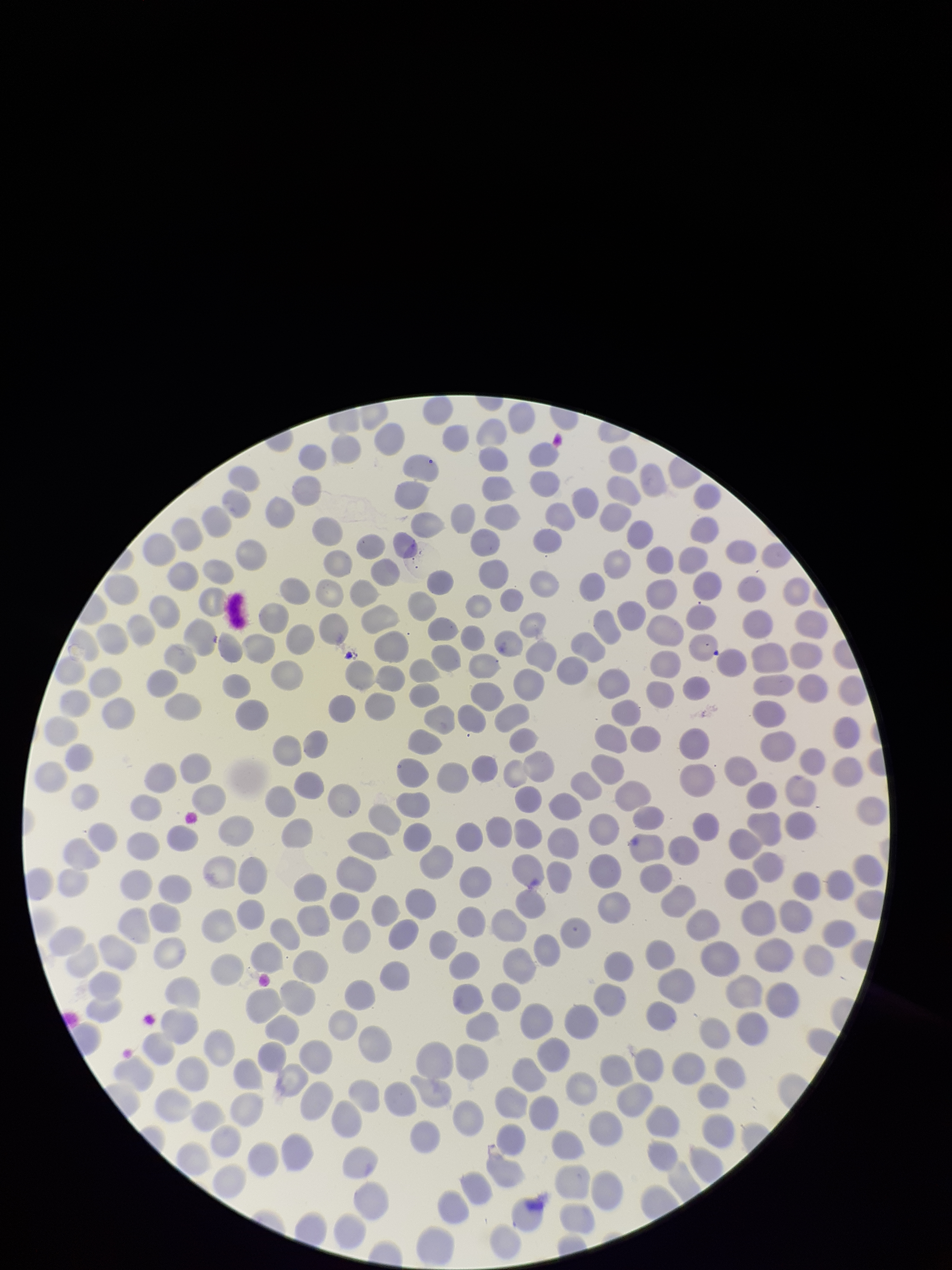

image size = 952×1270 pixels
capture = smartphone photograph through the microscope eyepiece
stain = Giemsa
species reported for this patient = Plasmodium vivax
patient malaria status = infected
field of view = one from this slide
parasitized red blood cell count = 0
parasitized red blood cells = none detected
preparation = thin blood smear
red blood cell count = 304